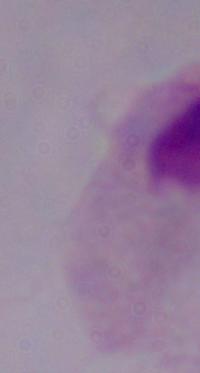
Summary:
  - Magnification: 1000x
  - Modality: micrograph
  - Identification: trichomonad